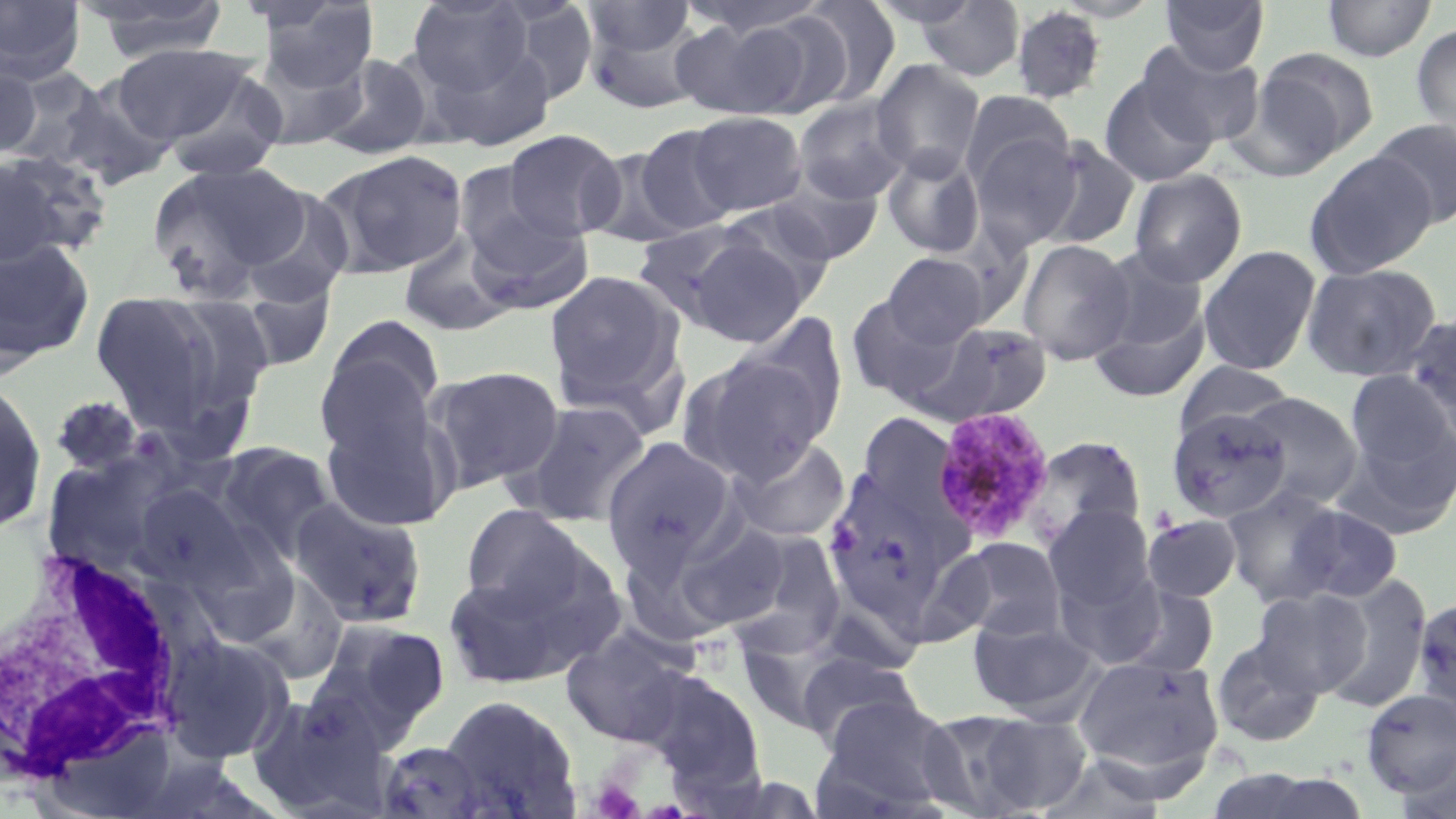

Approximate bounding boxes as named x1/y1/x2/y2 corners in pixels. White blood cell locations: (x1=3, y1=541, x2=211, y2=798). Uninfected red blood cell locations: (x1=81, y1=0, x2=231, y2=64), (x1=405, y1=0, x2=536, y2=100), (x1=678, y1=0, x2=831, y2=39), (x1=1159, y1=0, x2=1270, y2=74), (x1=1321, y1=0, x2=1436, y2=62), (x1=0, y1=1, x2=86, y2=83), (x1=253, y1=1, x2=381, y2=95), (x1=783, y1=1, x2=901, y2=109), (x1=914, y1=1, x2=1027, y2=81), (x1=582, y1=2, x2=698, y2=58), (x1=1009, y1=4, x2=1108, y2=106), (x1=581, y1=5, x2=709, y2=111), (x1=724, y1=6, x2=861, y2=117), (x1=672, y1=15, x2=815, y2=121), (x1=1411, y1=23, x2=1456, y2=145), (x1=1136, y1=41, x2=1264, y2=148), (x1=110, y1=43, x2=257, y2=145), (x1=1251, y1=46, x2=1379, y2=165), (x1=319, y1=53, x2=435, y2=160), (x1=0, y1=57, x2=43, y2=163), (x1=871, y1=58, x2=986, y2=180), (x1=0, y1=66, x2=126, y2=178), (x1=158, y1=70, x2=289, y2=183), (x1=38, y1=73, x2=182, y2=190), (x1=1100, y1=73, x2=1218, y2=187), (x1=960, y1=90, x2=1074, y2=193), (x1=792, y1=97, x2=911, y2=205), (x1=687, y1=111, x2=808, y2=216), (x1=1370, y1=119, x2=1456, y2=227), (x1=633, y1=124, x2=740, y2=236), (x1=502, y1=128, x2=625, y2=241), (x1=969, y1=131, x2=1082, y2=250), (x1=1038, y1=137, x2=1141, y2=251), (x1=585, y1=146, x2=694, y2=248), (x1=881, y1=147, x2=985, y2=260), (x1=318, y1=149, x2=469, y2=279), (x1=0, y1=150, x2=109, y2=268), (x1=1304, y1=150, x2=1438, y2=279), (x1=146, y1=160, x2=308, y2=302), (x1=1128, y1=169, x2=1247, y2=287), (x1=765, y1=174, x2=885, y2=265), (x1=238, y1=184, x2=356, y2=310), (x1=459, y1=193, x2=594, y2=314), (x1=714, y1=203, x2=840, y2=306), (x1=631, y1=219, x2=766, y2=331), (x1=398, y1=232, x2=516, y2=338), (x1=682, y1=235, x2=810, y2=347), (x1=0, y1=238, x2=95, y2=367), (x1=1018, y1=239, x2=1135, y2=365), (x1=1198, y1=244, x2=1322, y2=376), (x1=1094, y1=248, x2=1209, y2=354), (x1=883, y1=252, x2=989, y2=347), (x1=1300, y1=262, x2=1442, y2=383), (x1=543, y1=269, x2=686, y2=418), (x1=236, y1=280, x2=336, y2=372), (x1=88, y1=288, x2=242, y2=438), (x1=846, y1=294, x2=966, y2=407), (x1=1089, y1=302, x2=1210, y2=404), (x1=733, y1=309, x2=849, y2=440), (x1=315, y1=315, x2=447, y2=454), (x1=919, y1=321, x2=1052, y2=425), (x1=678, y1=350, x2=833, y2=482), (x1=1174, y1=361, x2=1297, y2=440), (x1=427, y1=364, x2=565, y2=491), (x1=1345, y1=371, x2=1454, y2=481), (x1=0, y1=377, x2=47, y2=532), (x1=317, y1=391, x2=460, y2=536), (x1=1238, y1=391, x2=1364, y2=508), (x1=50, y1=396, x2=145, y2=477), (x1=511, y1=399, x2=653, y2=527), (x1=1166, y1=408, x2=1292, y2=524), (x1=857, y1=411, x2=960, y2=524), (x1=1336, y1=419, x2=1455, y2=539), (x1=601, y1=435, x2=741, y2=574), (x1=1023, y1=435, x2=1147, y2=551), (x1=729, y1=436, x2=851, y2=543), (x1=212, y1=441, x2=340, y2=564), (x1=40, y1=445, x2=188, y2=580), (x1=821, y1=478, x2=959, y2=624), (x1=133, y1=484, x2=253, y2=590), (x1=1221, y1=485, x2=1347, y2=607), (x1=289, y1=495, x2=428, y2=629), (x1=460, y1=503, x2=593, y2=619), (x1=1284, y1=503, x2=1403, y2=604), (x1=1043, y1=506, x2=1157, y2=616), (x1=1142, y1=515, x2=1242, y2=602), (x1=674, y1=521, x2=796, y2=632), (x1=720, y1=528, x2=849, y2=654), (x1=188, y1=533, x2=299, y2=646), (x1=944, y1=537, x2=1068, y2=643), (x1=617, y1=544, x2=728, y2=649), (x1=1054, y1=561, x2=1168, y2=668), (x1=441, y1=567, x2=589, y2=691), (x1=238, y1=570, x2=349, y2=686), (x1=1315, y1=575, x2=1432, y2=711), (x1=1111, y1=581, x2=1221, y2=678), (x1=1251, y1=587, x2=1373, y2=697), (x1=1411, y1=596, x2=1456, y2=720), (x1=967, y1=614, x2=1101, y2=722), (x1=308, y1=617, x2=452, y2=743), (x1=560, y1=623, x2=700, y2=748), (x1=162, y1=633, x2=294, y2=763), (x1=1210, y1=634, x2=1325, y2=748), (x1=793, y1=650, x2=926, y2=752), (x1=1072, y1=655, x2=1223, y2=777), (x1=636, y1=669, x2=766, y2=791), (x1=1359, y1=689, x2=1456, y2=798), (x1=247, y1=693, x2=393, y2=817), (x1=440, y1=694, x2=583, y2=817), (x1=818, y1=696, x2=962, y2=814), (x1=916, y1=709, x2=1053, y2=818), (x1=970, y1=718, x2=1110, y2=815), (x1=374, y1=740, x2=494, y2=818), (x1=1393, y1=750, x2=1456, y2=819), (x1=1036, y1=753, x2=1173, y2=817). Platelet locations: (x1=591, y1=779, x2=645, y2=819). Plasmodium malariae-infected red blood cell locations: (x1=930, y1=406, x2=1056, y2=546). Slide-level diagnosis: Plasmodium malariae. May-Grünwald-Giemsa stain. One field of a larger specimen. Light microscopy. Image is 1456×819 pixels. 1000x magnification. Thin blood film.